Outline each blood parasite and name the species.
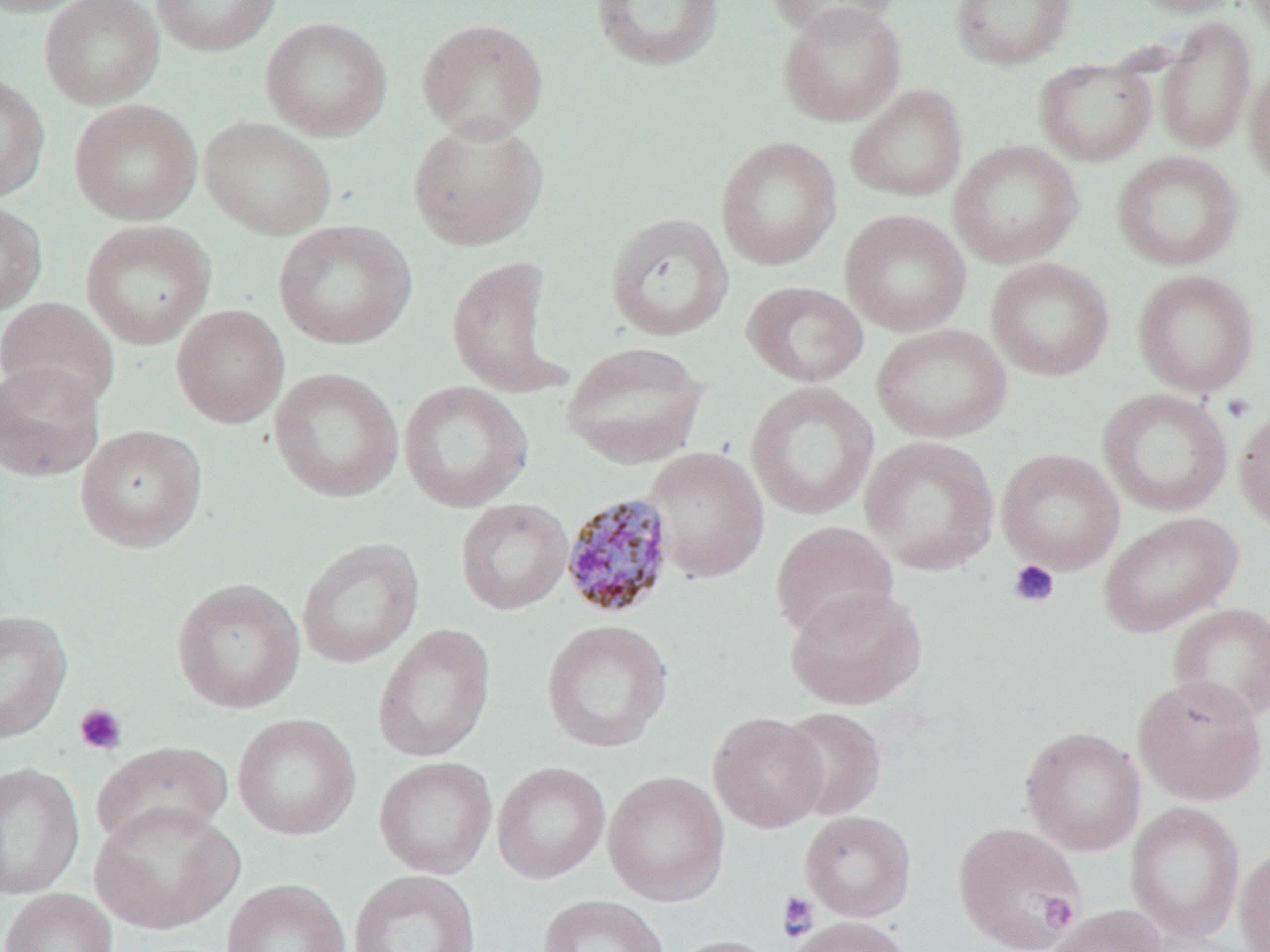

Approximate bounding boxes as (x1,y1)-(x2,y2) corner pairs in pixels.
Plasmodium malariae-infected red blood cells: (560,492)-(677,620).
No Plasmodium falciparum, Plasmodium ovale, Plasmodium vivax, Babesia divergens, or Trypanosoma brucei observed.

slide-level diagnosis = Plasmodium malariae
modality = optical microscopy
image size = 1270×952 pixels
preparation = thin blood smear
magnification = 1000x
uninfected red blood cell locations = approximate bounding boxes as (x1,y1)-(x2,y2) corner pairs in pixels: (0,0)-(91,17), (39,0)-(164,108), (151,0)-(281,56), (589,0)-(725,72), (765,0)-(902,41), (951,0)-(1076,70), (1125,0)-(1245,17), (778,3)-(906,125), (261,16)-(392,140), (1157,17)-(1256,153), (416,18)-(548,141), (1034,59)-(1156,166), (1245,61)-(1270,190), (0,74)-(50,202), (846,84)-(968,202), (69,99)-(202,225), (198,116)-(336,240), (407,116)-(548,251), (716,136)-(842,270), (949,139)-(1083,269), (1112,149)-(1245,271), (0,200)-(47,315), (840,209)-(972,336), (604,213)-(733,341), (80,219)-(215,348), (273,220)-(417,350), (446,255)-(567,398), (986,257)-(1115,381), (1133,269)-(1260,397), (742,280)-(868,387), (0,297)-(120,411), (171,304)-(289,428), (871,323)-(1012,444), (560,341)-(709,469), (0,361)-(104,482), (269,367)-(403,502), (398,380)-(533,512), (745,380)-(878,520), (1097,388)-(1233,516), (1235,406)-(1270,533), (75,424)-(206,551), (860,435)-(999,574), (642,446)-(770,582), (996,448)-(1125,574), (455,498)-(573,615), (1097,511)-(1243,637), (770,521)-(898,640), (296,537)-(424,668), (171,578)-(305,714), (785,586)-(927,710), (1167,601)-(1270,724), (0,610)-(72,744), (541,619)-(674,753), (372,624)-(495,763), (1132,674)-(1268,806), (777,706)-(886,820), (708,712)-(828,833), (232,713)-(361,841), (1020,725)-(1145,855), (90,741)-(234,849), (374,756)-(497,879), (492,761)-(611,884), (0,762)-(84,899), (603,770)-(730,906), (88,801)-(243,935), (1125,802)-(1246,945), (800,811)-(916,922), (953,821)-(1085,952), (1235,844)-(1270,952), (348,870)-(481,952), (221,879)-(350,952), (1,888)-(118,952), (537,894)-(670,952), (1046,904)-(1166,952), (785,916)-(915,952), (669,935)-(782,952)
stain = May-Grünwald-Giemsa
platelet locations = approximate bounding boxes as (x1,y1)-(x2,y2) corner pairs in pixels: (1221,393)-(1256,423), (1008,559)-(1060,608), (74,702)-(128,756), (950,818)-(1088,951), (777,892)-(819,941), (1039,893)-(1078,931)
field of view = single